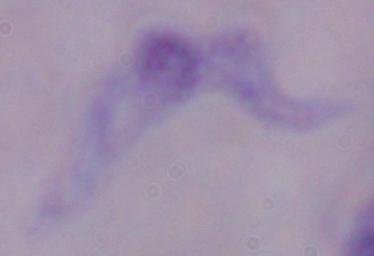 Captured at 1000x magnification. A trypanosome is seen. Micrograph.